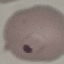

malaria_status: parasitized
image_type: cell patch, automatically extracted from a larger field of view and resized to 64 × 64 pixels
capture: smartphone through the microscope eyepiece
stain: Giemsa
preparation: thin blood smear